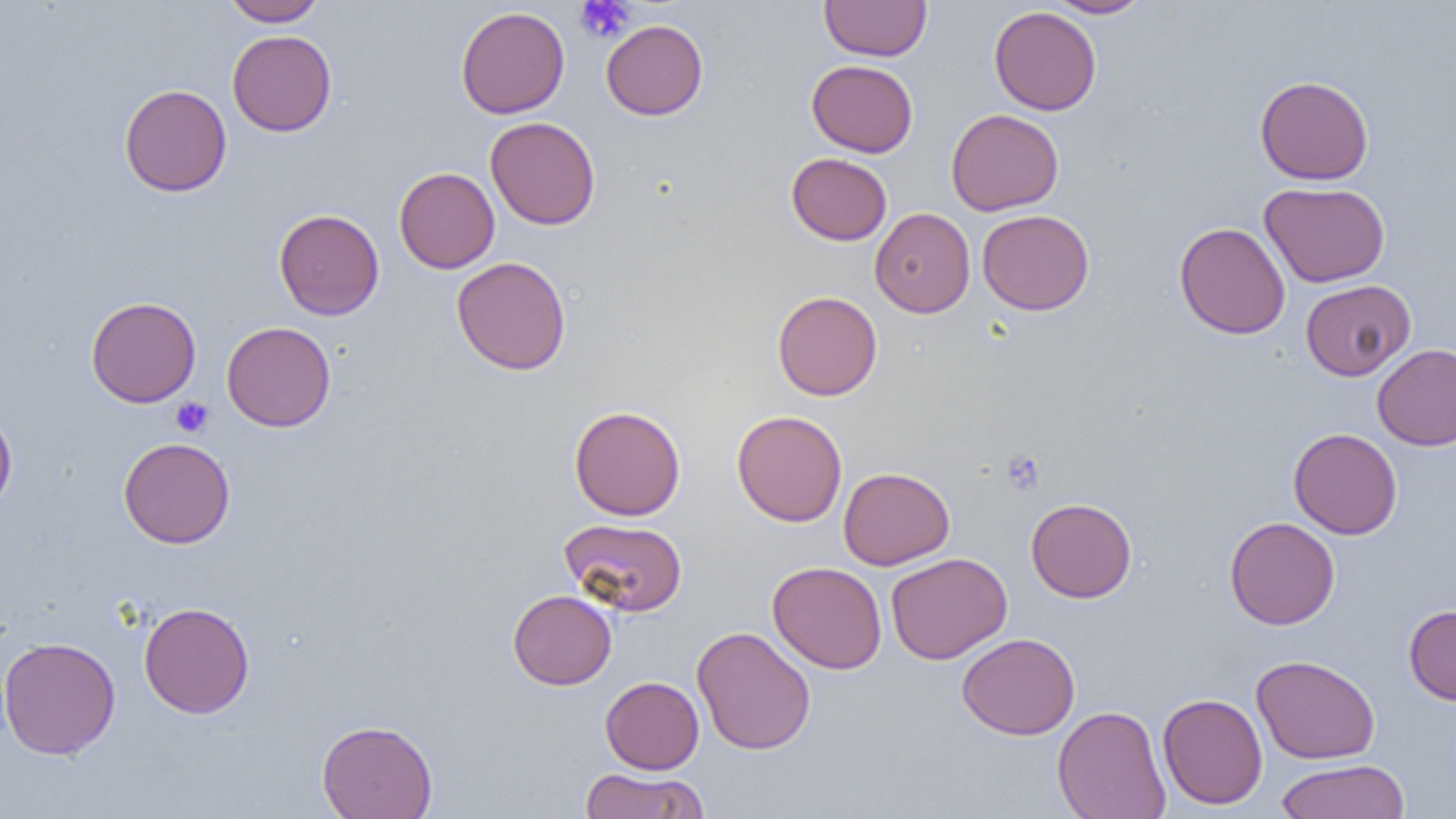

slide-level diagnosis = negative for blood parasites
magnification = 1000x
uninfected red blood cell locations = approximate bounding boxes as named x1/y1/x2/y2 corners in pixels: (x1=222, y1=0, x2=327, y2=26), (x1=1044, y1=0, x2=1153, y2=18), (x1=819, y1=1, x2=932, y2=61), (x1=455, y1=6, x2=569, y2=119), (x1=989, y1=6, x2=1102, y2=115), (x1=601, y1=19, x2=708, y2=120), (x1=227, y1=30, x2=336, y2=136), (x1=806, y1=59, x2=919, y2=157), (x1=1255, y1=75, x2=1374, y2=185), (x1=119, y1=84, x2=232, y2=197), (x1=945, y1=108, x2=1064, y2=215), (x1=485, y1=117, x2=600, y2=230), (x1=787, y1=152, x2=892, y2=245), (x1=394, y1=167, x2=500, y2=273), (x1=1259, y1=181, x2=1390, y2=287), (x1=870, y1=207, x2=975, y2=318), (x1=274, y1=208, x2=384, y2=320), (x1=977, y1=209, x2=1094, y2=315), (x1=1175, y1=223, x2=1290, y2=339), (x1=452, y1=256, x2=571, y2=375), (x1=1300, y1=279, x2=1416, y2=380), (x1=772, y1=291, x2=882, y2=400), (x1=85, y1=296, x2=201, y2=407), (x1=221, y1=321, x2=336, y2=432), (x1=1372, y1=344, x2=1456, y2=451), (x1=569, y1=405, x2=685, y2=520), (x1=0, y1=407, x2=17, y2=513), (x1=732, y1=410, x2=847, y2=526), (x1=1288, y1=428, x2=1402, y2=539), (x1=118, y1=437, x2=235, y2=548), (x1=838, y1=466, x2=955, y2=570), (x1=1026, y1=497, x2=1137, y2=602), (x1=1224, y1=516, x2=1340, y2=630), (x1=559, y1=517, x2=687, y2=616), (x1=886, y1=553, x2=1012, y2=664), (x1=768, y1=561, x2=887, y2=674), (x1=508, y1=589, x2=617, y2=690), (x1=138, y1=601, x2=255, y2=719), (x1=1404, y1=604, x2=1456, y2=705), (x1=691, y1=626, x2=816, y2=755), (x1=957, y1=633, x2=1080, y2=740), (x1=0, y1=637, x2=120, y2=759), (x1=1251, y1=655, x2=1380, y2=764), (x1=600, y1=676, x2=704, y2=774), (x1=1157, y1=692, x2=1268, y2=809), (x1=1052, y1=705, x2=1171, y2=819), (x1=316, y1=719, x2=438, y2=819), (x1=1274, y1=759, x2=1410, y2=819), (x1=578, y1=768, x2=709, y2=818)
preparation = thin blood smear
modality = optical microscopy
image size = 1456×819 pixels
field of view = single
platelet locations = approximate bounding boxes as named x1/y1/x2/y2 corners in pixels: (x1=575, y1=0, x2=635, y2=43), (x1=170, y1=397, x2=213, y2=437), (x1=1001, y1=450, x2=1045, y2=495)